Look for Plasmodium parasites.
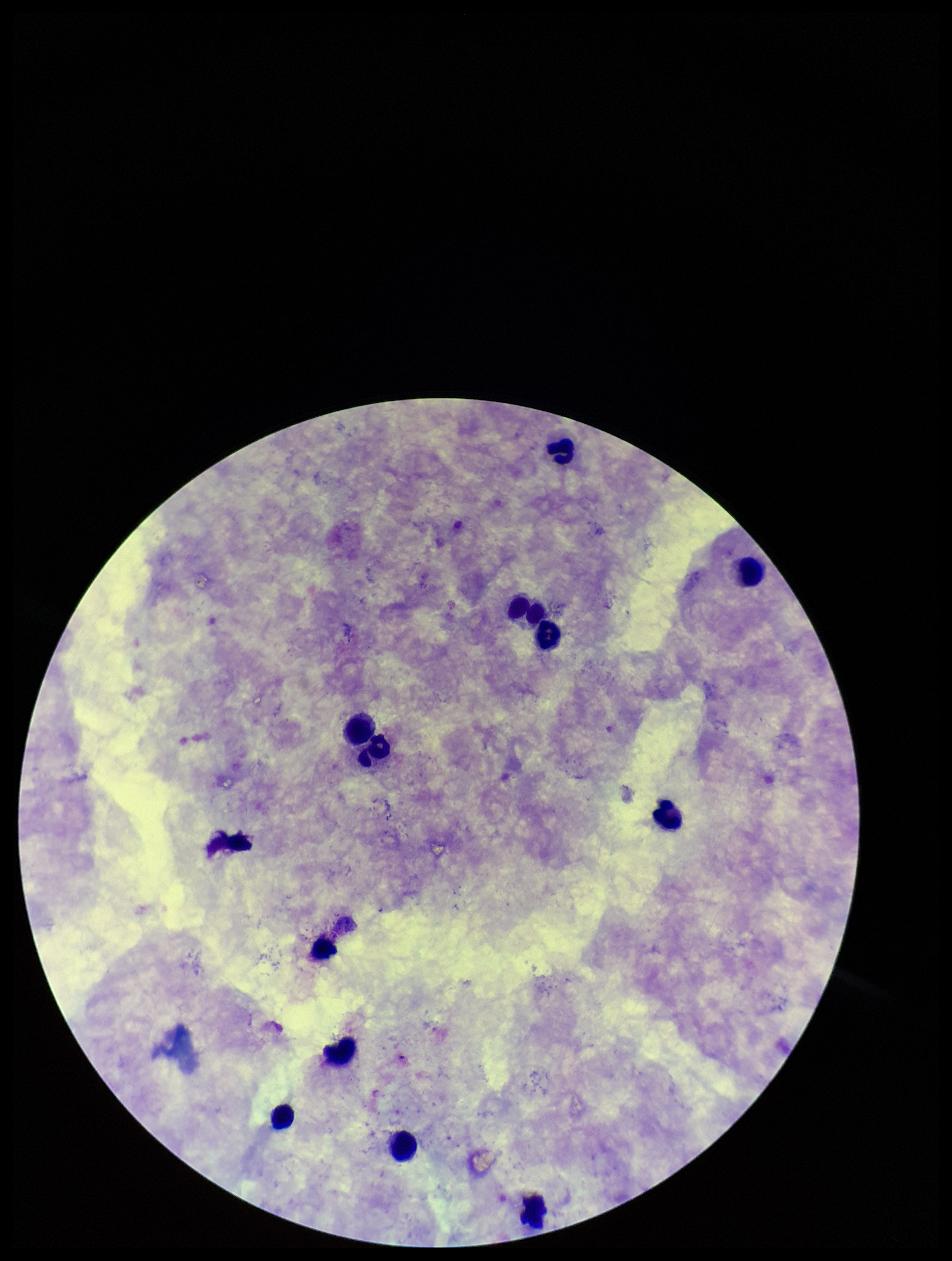

None identified.

{
  "field_of_view": "one from this slide",
  "capture": "smartphone photograph through the microscope eyepiece",
  "stain": "Giemsa",
  "patient_malaria_status": "negative",
  "parasite_count": 0,
  "image_size": "952×1261 pixels",
  "preparation": "thick smear",
  "leukocyte_count": 12
}